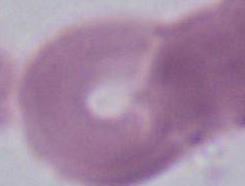
Summary:
  - Identification: red blood cell
  - Modality: micrograph
  - Magnification: 1000x